Identify the parasite.
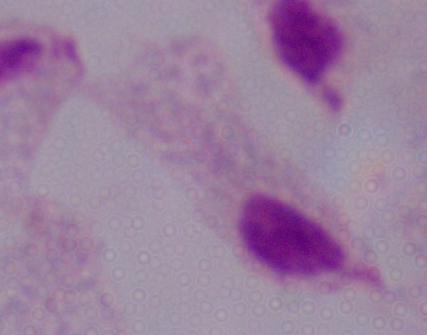
A trichomonad.

Photomicrograph. 1000x magnification.